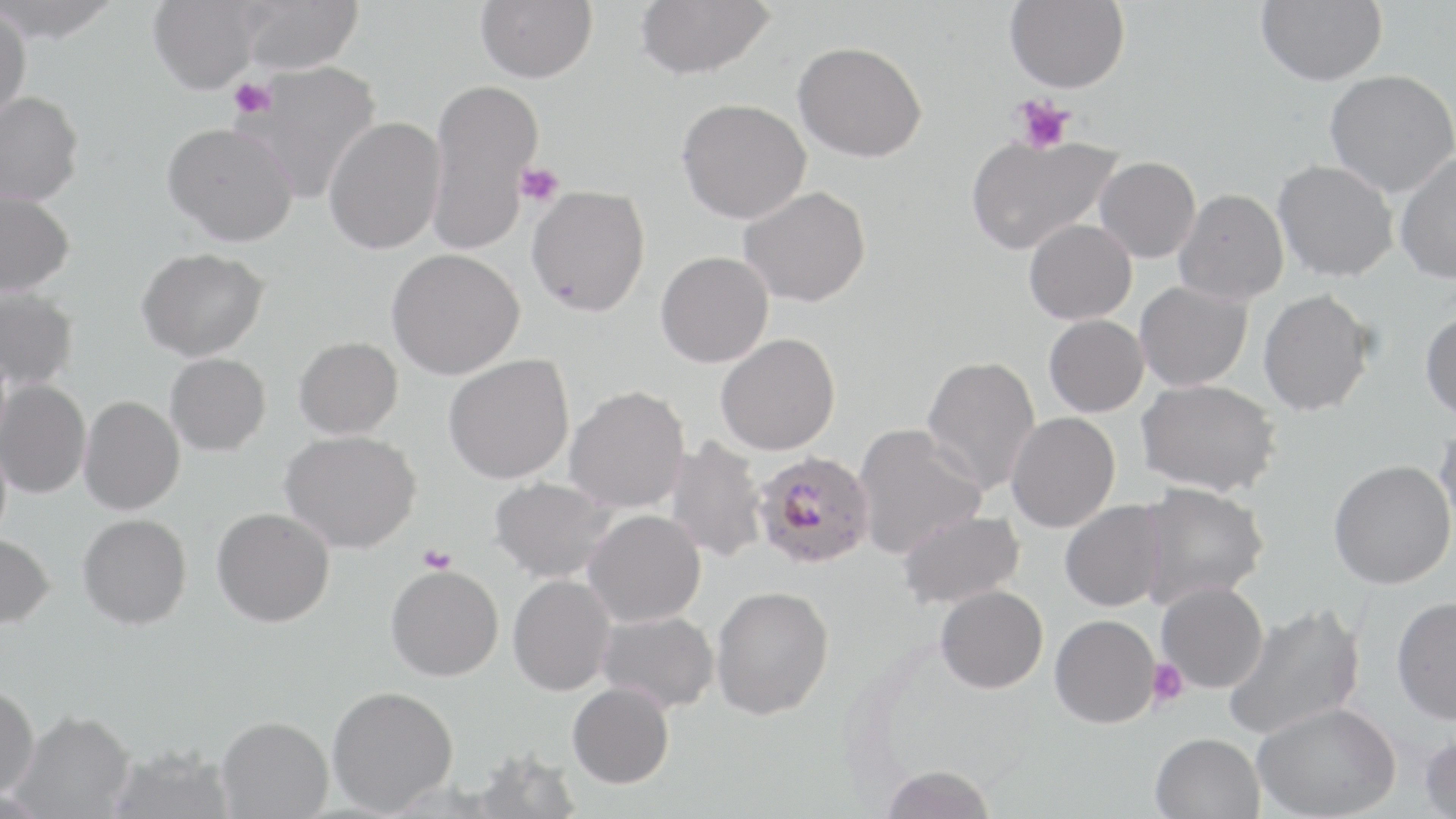

Approximate bounding boxes as [x1, y1, x2, y2] in pixels. Plasmodium falciparum-infected red blood cell locations: [753, 451, 874, 568]. Uninfected red blood cell locations: [0, 0, 124, 46], [148, 0, 265, 97], [238, 0, 365, 75], [476, 0, 597, 83], [635, 0, 775, 80], [1005, 0, 1130, 93], [1255, 0, 1387, 86], [0, 7, 32, 125], [792, 40, 927, 162], [240, 59, 383, 203], [1323, 69, 1455, 197], [427, 77, 544, 254], [0, 92, 85, 208], [676, 98, 810, 223], [323, 117, 446, 255], [162, 124, 299, 248], [965, 133, 1121, 255], [1394, 152, 1456, 284], [1094, 156, 1200, 263], [1272, 159, 1399, 282], [526, 185, 650, 316], [738, 185, 870, 307], [1174, 188, 1289, 305], [0, 191, 75, 297], [1024, 218, 1136, 324], [137, 248, 269, 361], [387, 248, 525, 379], [655, 251, 773, 367], [1134, 281, 1252, 392], [0, 286, 79, 389], [1257, 289, 1375, 416], [1420, 310, 1456, 421], [1043, 315, 1148, 417], [715, 333, 840, 455], [294, 336, 403, 440], [165, 353, 271, 456], [443, 354, 574, 484], [920, 354, 1041, 497], [0, 378, 91, 500], [1135, 378, 1279, 496], [564, 386, 689, 514], [79, 396, 185, 515], [1006, 412, 1120, 533], [1433, 418, 1456, 544], [852, 423, 986, 558], [280, 430, 422, 554], [665, 437, 768, 563], [1328, 459, 1455, 590], [489, 477, 618, 582], [1136, 482, 1268, 608], [1060, 499, 1168, 612], [212, 507, 335, 628], [583, 509, 705, 627], [896, 509, 1025, 609], [78, 513, 192, 630], [0, 534, 55, 631], [386, 564, 504, 681], [508, 574, 616, 695], [1156, 581, 1268, 693], [711, 585, 834, 720], [935, 585, 1048, 693], [1391, 596, 1456, 725], [1222, 603, 1366, 740], [597, 610, 719, 713], [1050, 614, 1160, 728], [568, 682, 674, 789], [0, 685, 40, 798], [327, 685, 458, 815], [1251, 702, 1401, 819], [10, 711, 135, 818], [217, 716, 334, 818], [1150, 732, 1264, 819], [1418, 732, 1456, 819], [107, 745, 235, 819], [472, 747, 582, 819], [880, 764, 997, 819]. Platelet locations: [228, 78, 277, 120], [1011, 96, 1074, 154], [515, 163, 565, 206], [418, 544, 457, 573], [1147, 659, 1189, 706]. Slide-level diagnosis: Plasmodium falciparum. One field of a larger specimen. Light microscopy. May-Grünwald-Giemsa stain. Thin blood smear. Captured at 1000x magnification. Image is 1456×819 pixels.